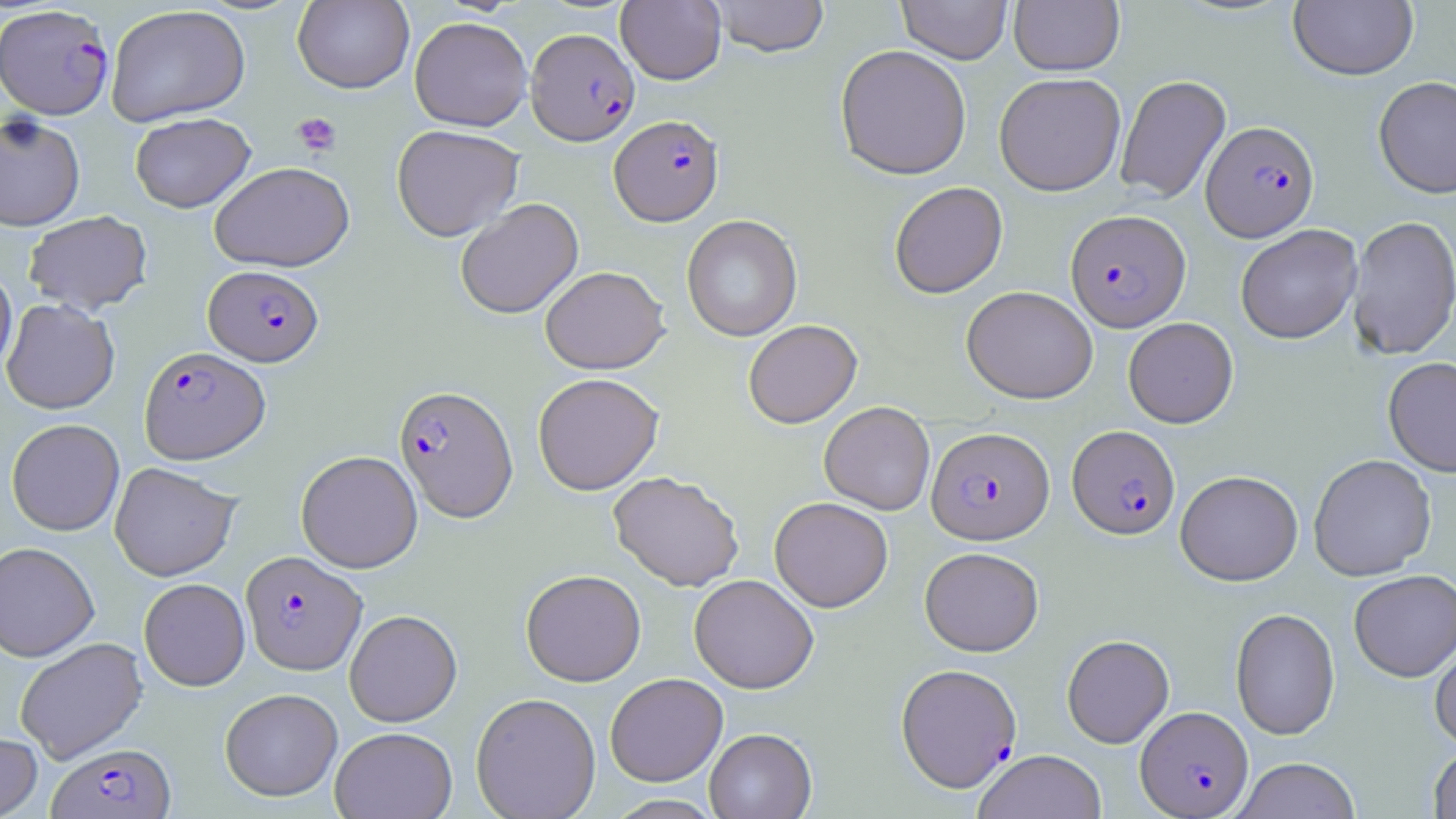

Summary:
  - Coordinate format: approximate bounding boxes as [x1, y1, x2, y2] in pixels
  - Uninfected red blood cell locations: [616, 0, 726, 85], [709, 0, 830, 57], [897, 0, 1012, 64], [292, 1, 414, 93], [1009, 1, 1124, 75], [1289, 1, 1418, 81], [105, 5, 251, 126], [409, 16, 532, 131], [834, 44, 972, 180], [993, 72, 1126, 196], [1115, 74, 1231, 204], [1373, 76, 1456, 198], [129, 112, 255, 213], [0, 113, 85, 232], [391, 124, 524, 242], [209, 161, 355, 272], [889, 181, 1008, 298], [455, 198, 583, 319], [23, 210, 153, 315], [681, 214, 803, 342], [1347, 215, 1456, 360], [1235, 224, 1362, 344], [0, 264, 17, 377], [540, 266, 669, 374], [961, 285, 1098, 404], [1, 298, 120, 414], [1123, 317, 1238, 428], [743, 319, 862, 428], [1383, 356, 1456, 477], [533, 372, 664, 495], [819, 402, 935, 515], [6, 418, 124, 535], [296, 450, 423, 573], [1308, 454, 1436, 581], [109, 462, 242, 581], [1175, 470, 1303, 586], [608, 471, 744, 591], [769, 496, 893, 612], [0, 541, 99, 661], [920, 547, 1044, 656], [520, 569, 646, 686], [1348, 570, 1456, 682], [689, 573, 818, 693], [139, 578, 250, 690], [1230, 608, 1340, 740], [344, 609, 462, 726], [1062, 634, 1174, 747], [14, 637, 147, 763], [1430, 637, 1456, 749], [605, 673, 727, 786], [220, 687, 343, 801], [471, 692, 601, 819], [330, 726, 457, 818], [704, 728, 816, 819], [0, 732, 42, 819], [1428, 745, 1456, 818], [972, 749, 1107, 819], [1233, 758, 1361, 819], [603, 794, 725, 819]
  - Platelet locations: [292, 112, 342, 157]
  - Plasmodium falciparum-infected red blood cell locations: [0, 3, 115, 119], [526, 28, 639, 145], [609, 114, 724, 226], [1201, 120, 1319, 241], [1065, 209, 1190, 332], [203, 264, 324, 366], [139, 346, 270, 464], [394, 384, 518, 522], [1067, 424, 1180, 540], [927, 426, 1054, 544], [240, 550, 367, 675], [896, 662, 1022, 791], [1136, 705, 1253, 817], [48, 742, 175, 819]
  - Slide-level diagnosis: Plasmodium falciparum
  - Stain: May-Grünwald-Giemsa
  - Preparation: thin blood smear
  - Magnification: 1000x
  - Modality: light microscopy
  - Image size: 1456×819 pixels
  - Field of view: one of a larger specimen